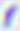
modality = micrograph
identification = Toxoplasma gondii
magnification = 400x